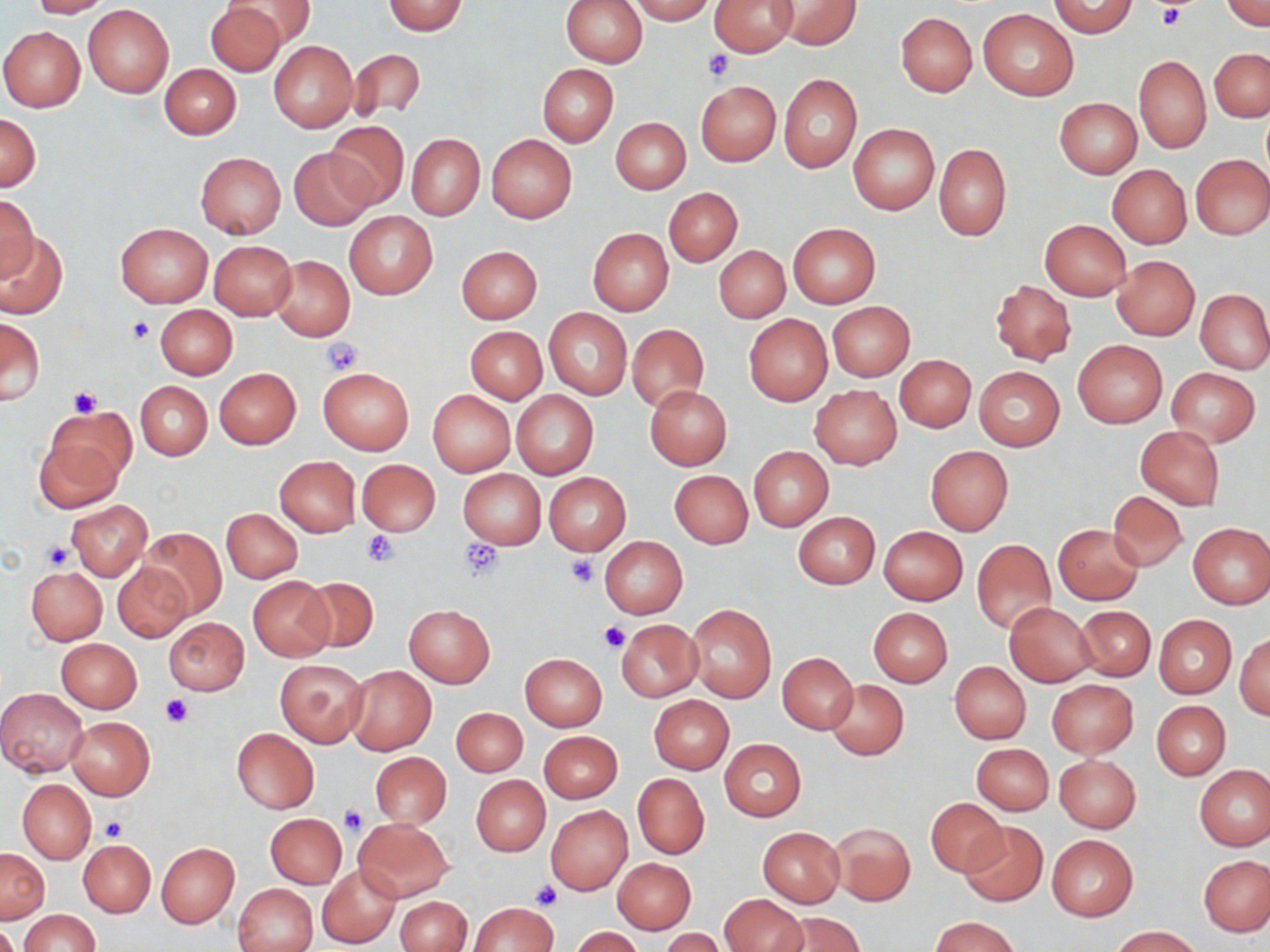
Approximate bounding boxes as [x1, y1, x2, y2] in pixels. Platelet locations: [1157, 5, 1188, 30], [702, 48, 734, 82], [126, 316, 154, 344], [321, 338, 362, 376], [67, 385, 102, 418], [361, 531, 401, 567], [458, 538, 504, 583], [40, 540, 75, 571], [567, 555, 599, 587], [599, 621, 630, 654], [160, 693, 193, 727], [338, 804, 368, 837], [100, 817, 128, 841], [530, 881, 561, 911]. Uninfected red blood cell locations: [27, 0, 111, 18], [227, 0, 315, 49], [560, 0, 647, 68], [627, 0, 713, 23], [708, 0, 799, 56], [773, 0, 859, 49], [1048, 1, 1138, 38], [1223, 1, 1270, 30], [204, 2, 288, 76], [382, 2, 469, 35], [83, 5, 174, 98], [979, 8, 1078, 101], [896, 12, 977, 97], [0, 26, 86, 111], [269, 40, 358, 132], [348, 49, 425, 121], [1210, 49, 1270, 121], [1133, 54, 1210, 153], [160, 63, 241, 139], [537, 64, 618, 146], [779, 75, 861, 172], [695, 81, 780, 166], [1055, 98, 1141, 178], [0, 111, 40, 190], [611, 117, 691, 194], [327, 122, 408, 207], [849, 123, 939, 215], [407, 134, 484, 220], [486, 135, 576, 222], [933, 143, 1011, 240], [290, 146, 377, 230], [195, 152, 285, 237], [1191, 154, 1270, 239], [1108, 164, 1191, 249], [664, 187, 742, 266], [2, 193, 38, 282], [345, 211, 437, 298], [1039, 218, 1131, 301], [115, 221, 213, 307], [787, 222, 881, 308], [588, 228, 674, 316], [0, 231, 69, 320], [208, 240, 296, 321], [456, 245, 542, 323], [714, 246, 790, 322], [270, 256, 355, 341], [1112, 256, 1200, 341], [990, 281, 1075, 365], [1196, 289, 1270, 373], [826, 301, 914, 381], [155, 304, 237, 379], [545, 308, 632, 399], [743, 314, 832, 405], [1, 317, 45, 403], [627, 324, 707, 411], [466, 327, 547, 403], [1072, 339, 1168, 429], [895, 354, 976, 433], [974, 366, 1065, 451], [214, 367, 301, 449], [318, 367, 414, 454], [1166, 367, 1260, 447], [136, 381, 212, 460], [645, 385, 732, 470], [810, 385, 902, 469], [428, 390, 515, 475], [511, 390, 599, 478], [41, 406, 133, 504], [1135, 426, 1224, 511], [925, 446, 1013, 535], [749, 447, 833, 531], [275, 456, 361, 536], [357, 459, 440, 536], [458, 469, 546, 547], [669, 470, 753, 548], [543, 472, 631, 555], [1108, 491, 1187, 571], [67, 500, 152, 580], [221, 508, 302, 582], [792, 511, 880, 589], [1188, 522, 1270, 609], [1053, 523, 1144, 605], [879, 526, 968, 606], [142, 529, 226, 619], [600, 536, 688, 618], [608, 537, 693, 698], [972, 540, 1056, 633], [112, 562, 192, 641], [27, 566, 107, 644], [248, 577, 333, 661], [301, 577, 379, 653], [1005, 601, 1097, 688], [404, 604, 495, 688], [687, 604, 776, 703], [1073, 605, 1155, 681], [869, 608, 953, 687], [1153, 615, 1235, 698], [163, 617, 250, 695], [615, 618, 703, 701], [1235, 633, 1270, 720], [55, 638, 142, 714], [520, 652, 606, 731], [777, 653, 858, 733], [275, 658, 368, 748], [949, 661, 1030, 744], [345, 665, 436, 754], [825, 678, 909, 760], [1046, 680, 1138, 758], [0, 688, 89, 777], [649, 695, 734, 773], [1151, 700, 1231, 779], [451, 707, 527, 777], [65, 716, 155, 800], [231, 728, 318, 813], [538, 731, 622, 803], [720, 739, 805, 821], [972, 744, 1053, 815], [370, 752, 452, 827], [1055, 754, 1141, 831], [1195, 765, 1270, 851], [633, 773, 709, 859], [471, 775, 550, 855], [17, 779, 96, 863], [925, 797, 1008, 877], [546, 805, 633, 896], [265, 814, 347, 888], [353, 818, 453, 901], [958, 821, 1047, 908], [830, 822, 915, 906], [758, 826, 844, 908], [1047, 834, 1138, 920], [78, 840, 155, 916], [156, 843, 239, 928], [1, 848, 49, 922], [1199, 854, 1270, 936], [612, 857, 696, 934], [316, 863, 401, 949], [232, 883, 317, 952], [720, 895, 807, 952], [396, 896, 471, 952], [469, 902, 558, 951], [20, 909, 99, 952], [779, 912, 864, 952], [931, 916, 1020, 952], [0, 921, 19, 952], [1111, 926, 1201, 951], [570, 927, 644, 952], [662, 929, 726, 952]. Slide-level diagnosis: no evidence of blood parasites. Thin blood film. Light microscopy. Image is 1270×952 pixels. May-Grünwald-Giemsa stain. 1000x magnification. One field of a larger specimen.